Assess the morphology of the red blood cells.
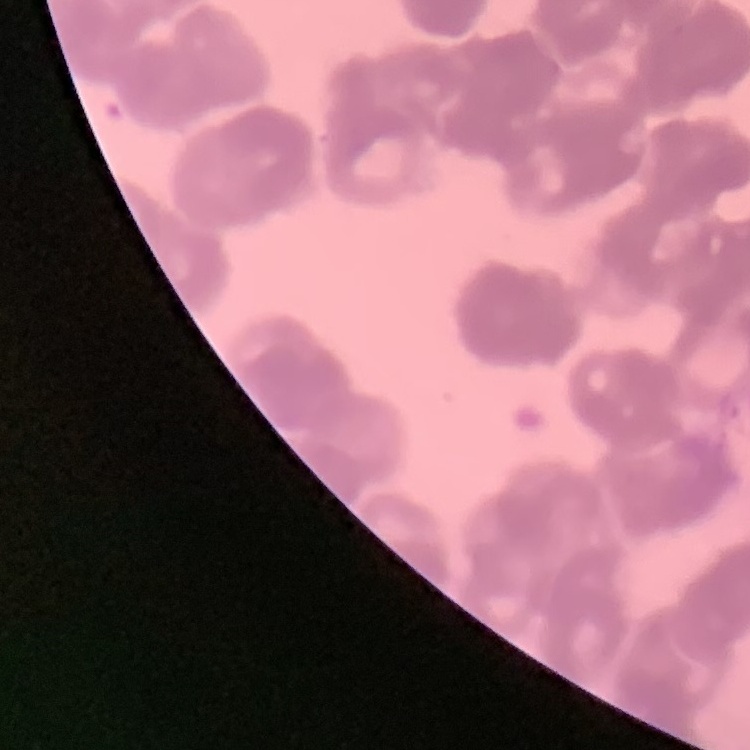
Rouleaux formation.

Square crop of a larger photomicrograph. Field's or Giemsa stain. Thin blood film.